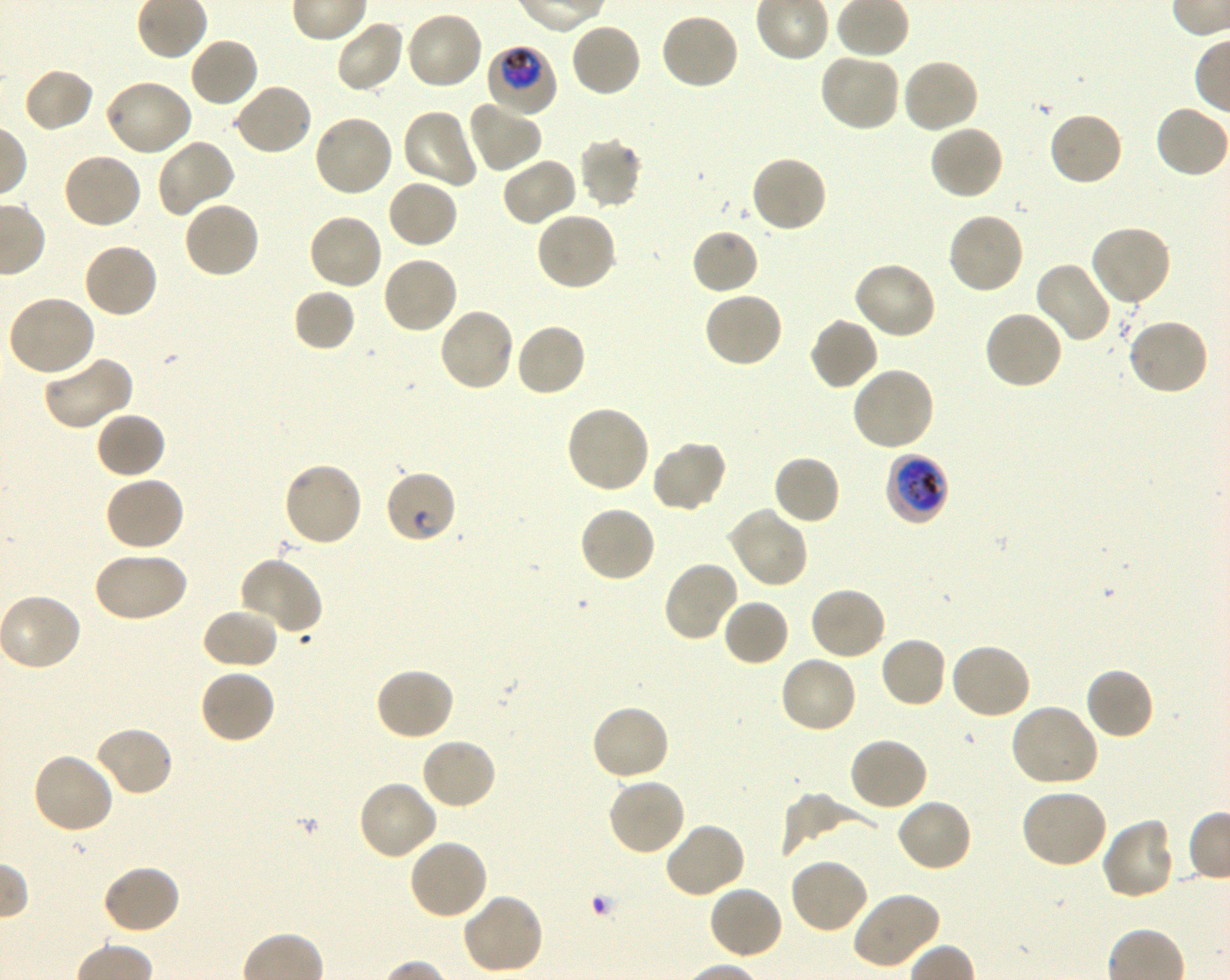

Approximate bounding boxes as [x1, y1, x2, y2] in pixels. Not every red blood cell is marked. A life-cycle stage — or a range of stages, where the recorded stages span more than one — follows each staged infected red blood cell.
Summary:
  - Locations of red blood cells of indeterminate infection status: [383, 468, 457, 545]
  - Locations of uninfected red blood cells: [405, 10, 485, 91], [659, 12, 740, 91], [335, 18, 404, 94], [569, 22, 642, 99], [188, 36, 259, 108], [817, 52, 901, 133], [900, 57, 981, 135], [21, 67, 96, 135], [103, 79, 194, 158], [232, 83, 314, 157], [467, 97, 543, 174], [1154, 103, 1230, 179], [400, 107, 479, 190], [1048, 111, 1124, 188], [312, 113, 394, 198], [928, 123, 1004, 200], [577, 136, 643, 210], [156, 139, 236, 218], [61, 152, 143, 230], [750, 154, 829, 234], [501, 157, 579, 227], [386, 178, 459, 249], [182, 199, 260, 279], [535, 210, 617, 292], [947, 211, 1025, 296], [307, 212, 385, 291], [1089, 223, 1173, 307], [690, 228, 760, 296], [82, 241, 160, 318], [381, 254, 459, 335], [852, 260, 938, 340], [1032, 260, 1112, 344], [292, 287, 356, 352], [702, 290, 785, 368], [7, 295, 96, 378], [438, 306, 515, 393], [983, 308, 1065, 390], [808, 317, 880, 392], [1126, 317, 1210, 397], [514, 321, 588, 397], [41, 355, 133, 431], [851, 365, 936, 452], [564, 403, 652, 495], [94, 411, 167, 480], [650, 441, 727, 512], [772, 454, 842, 526], [282, 460, 364, 548], [103, 474, 185, 553], [579, 503, 657, 584], [728, 507, 809, 588], [91, 549, 188, 624], [237, 556, 322, 634], [662, 560, 741, 642], [808, 585, 887, 661], [721, 597, 790, 667], [201, 607, 279, 670], [879, 635, 948, 709], [949, 641, 1032, 720], [778, 655, 859, 735], [1083, 666, 1155, 740], [373, 667, 456, 742], [198, 668, 278, 745], [590, 703, 672, 781], [1009, 703, 1099, 789], [93, 725, 175, 798], [847, 736, 928, 812], [419, 737, 497, 811], [30, 751, 115, 835], [607, 777, 687, 857], [357, 779, 438, 862], [1019, 787, 1109, 869], [780, 793, 876, 855], [895, 798, 973, 873], [1100, 816, 1175, 901], [663, 821, 747, 899], [407, 837, 489, 921], [788, 857, 869, 935], [101, 863, 182, 935], [708, 885, 784, 961], [852, 891, 941, 969], [462, 892, 545, 976]
  - Locations of infected red blood cells: [485, 46, 558, 118] trophozoite; [885, 452, 949, 526] trophozoite
  - Donor blood group: O+
  - Objective: 100x, oil immersion, numerical aperture 1.30
  - Stain: Giemsa
  - Field of view: one from this slide
  - Culture: in-vitro Plasmodium falciparum strain 3D7, shaking
  - Image size: 1230×980 pixels
  - Preparation: thin blood smear